Report the malaria status of this cell.
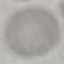
It is uninfected.

Giemsa-stained preparation. Photographed with a smartphone camera at the microscope eyepiece. Automatically extracted cell patch, resized to 64 × 64 pixels. Thin blood smear.